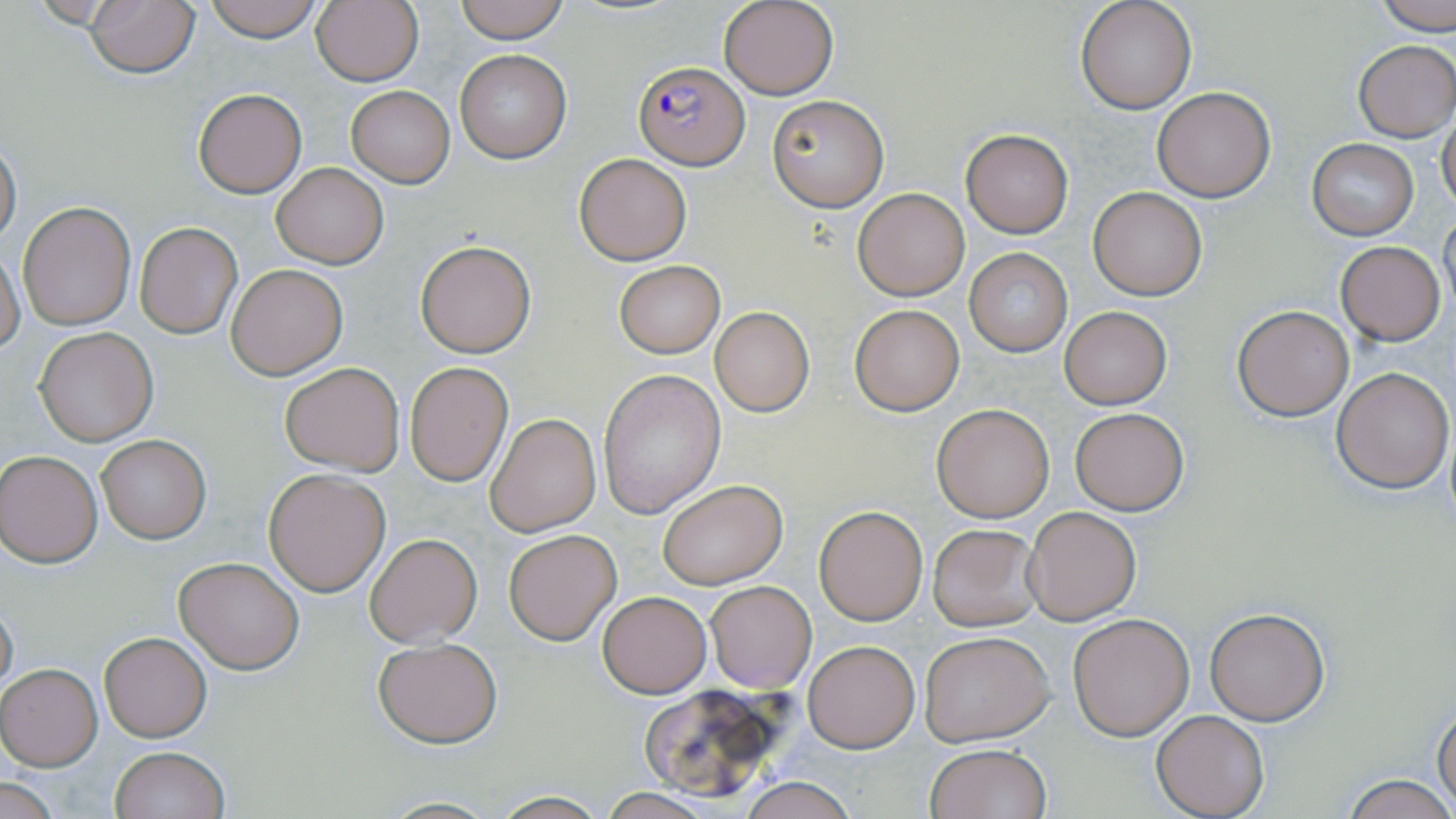
Approximate bounding boxes as named x1/y1/x2/y2 corners in pixels. Plasmodium falciparum-infected red blood cell locations: (x1=632, y1=61, x2=750, y2=169). Uninfected red blood cell locations: (x1=85, y1=0, x2=199, y2=79), (x1=201, y1=0, x2=328, y2=42), (x1=311, y1=0, x2=424, y2=87), (x1=455, y1=0, x2=570, y2=43), (x1=719, y1=0, x2=837, y2=100), (x1=1075, y1=0, x2=1197, y2=114), (x1=1371, y1=0, x2=1456, y2=35), (x1=1353, y1=39, x2=1456, y2=141), (x1=454, y1=49, x2=572, y2=164), (x1=347, y1=86, x2=455, y2=186), (x1=1150, y1=87, x2=1274, y2=202), (x1=192, y1=88, x2=308, y2=198), (x1=767, y1=94, x2=889, y2=211), (x1=1438, y1=112, x2=1456, y2=217), (x1=959, y1=129, x2=1073, y2=238), (x1=0, y1=136, x2=22, y2=247), (x1=1307, y1=140, x2=1419, y2=238), (x1=574, y1=153, x2=691, y2=264), (x1=272, y1=164, x2=387, y2=268), (x1=1088, y1=186, x2=1207, y2=300), (x1=853, y1=188, x2=969, y2=301), (x1=18, y1=202, x2=136, y2=331), (x1=1438, y1=209, x2=1456, y2=321), (x1=135, y1=222, x2=242, y2=339), (x1=415, y1=241, x2=536, y2=357), (x1=1335, y1=241, x2=1445, y2=345), (x1=0, y1=249, x2=25, y2=353), (x1=964, y1=249, x2=1072, y2=355), (x1=613, y1=260, x2=724, y2=358), (x1=226, y1=264, x2=347, y2=380), (x1=850, y1=305, x2=964, y2=416), (x1=1232, y1=305, x2=1355, y2=420), (x1=1059, y1=306, x2=1171, y2=410), (x1=710, y1=308, x2=815, y2=419), (x1=34, y1=327, x2=158, y2=446), (x1=279, y1=360, x2=405, y2=475), (x1=405, y1=362, x2=513, y2=487), (x1=1331, y1=367, x2=1454, y2=495), (x1=596, y1=369, x2=725, y2=519), (x1=930, y1=403, x2=1055, y2=521), (x1=1069, y1=407, x2=1189, y2=515), (x1=485, y1=412, x2=600, y2=538), (x1=94, y1=432, x2=212, y2=545), (x1=1, y1=450, x2=103, y2=567), (x1=263, y1=467, x2=391, y2=596), (x1=657, y1=478, x2=788, y2=589), (x1=813, y1=504, x2=928, y2=626), (x1=1024, y1=505, x2=1144, y2=626), (x1=928, y1=524, x2=1042, y2=632), (x1=503, y1=529, x2=620, y2=644), (x1=365, y1=533, x2=483, y2=647), (x1=174, y1=555, x2=305, y2=674), (x1=705, y1=579, x2=818, y2=692), (x1=598, y1=591, x2=711, y2=698), (x1=0, y1=593, x2=18, y2=701), (x1=1205, y1=607, x2=1330, y2=726), (x1=1067, y1=612, x2=1194, y2=740), (x1=919, y1=630, x2=1056, y2=745), (x1=97, y1=631, x2=212, y2=742), (x1=373, y1=638, x2=503, y2=747), (x1=803, y1=640, x2=920, y2=752), (x1=0, y1=663, x2=103, y2=770), (x1=635, y1=682, x2=799, y2=801), (x1=1433, y1=705, x2=1456, y2=812), (x1=1152, y1=710, x2=1268, y2=818), (x1=923, y1=743, x2=1053, y2=819), (x1=109, y1=747, x2=230, y2=819), (x1=1342, y1=774, x2=1455, y2=819), (x1=734, y1=777, x2=862, y2=819), (x1=1, y1=778, x2=62, y2=817), (x1=488, y1=792, x2=610, y2=819). Slide-level diagnosis: Plasmodium falciparum. Captured at 1000x magnification. Single field of view. Image is 1456×819 pixels. Thin blood film. May-Grünwald-Giemsa stain. Light microscopy.